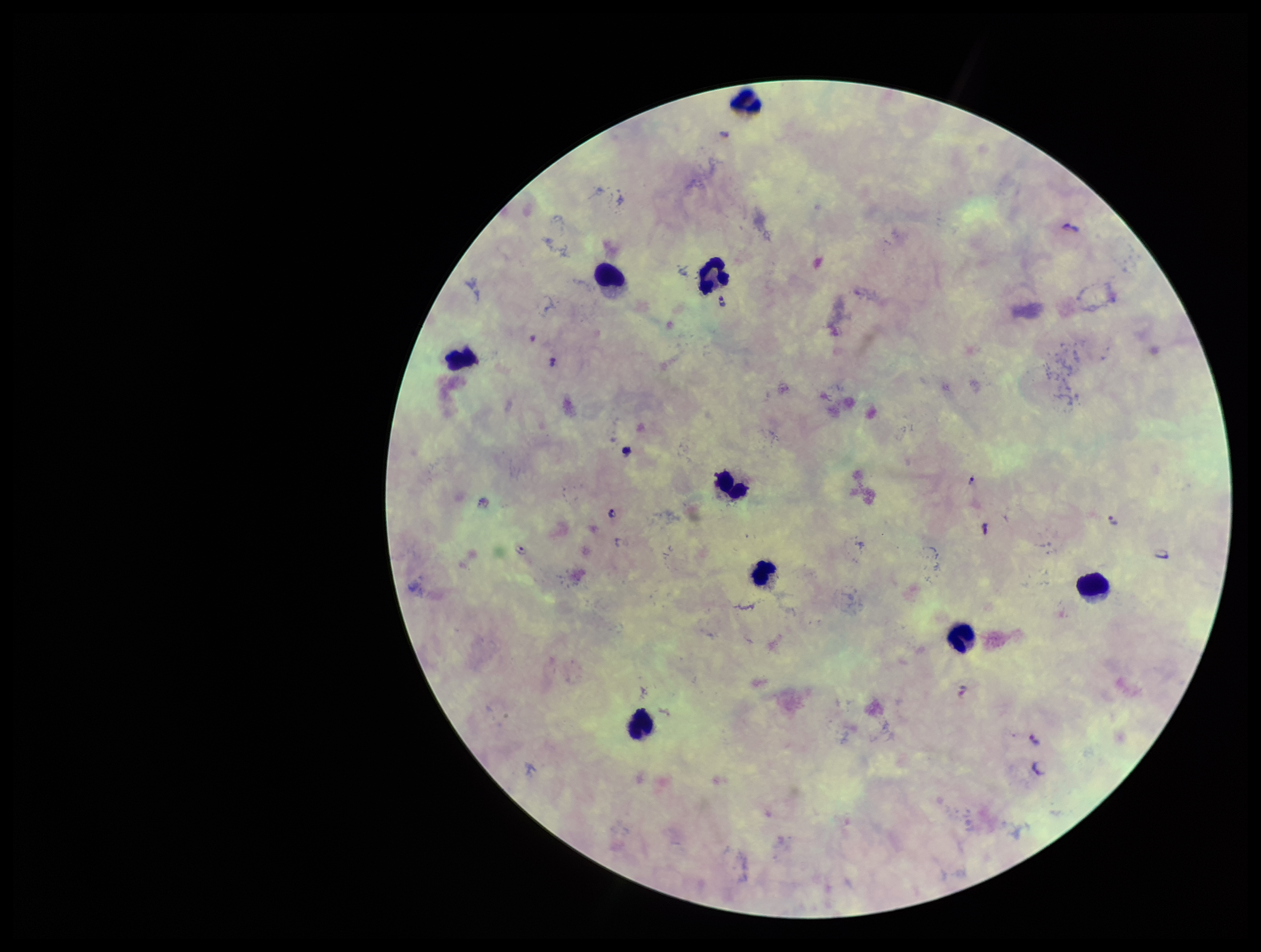 Preparation: thick smear. Leukocyte count: 9. Species reported for this patient: Plasmodium falciparum. Parasite count: 8. Plasmodium parasites: detected. Smartphone photograph taken through the eyepiece of a microscope. Stained with Giemsa. Image is 1261×952 pixels. Patient malaria status: infected. Single field of view.